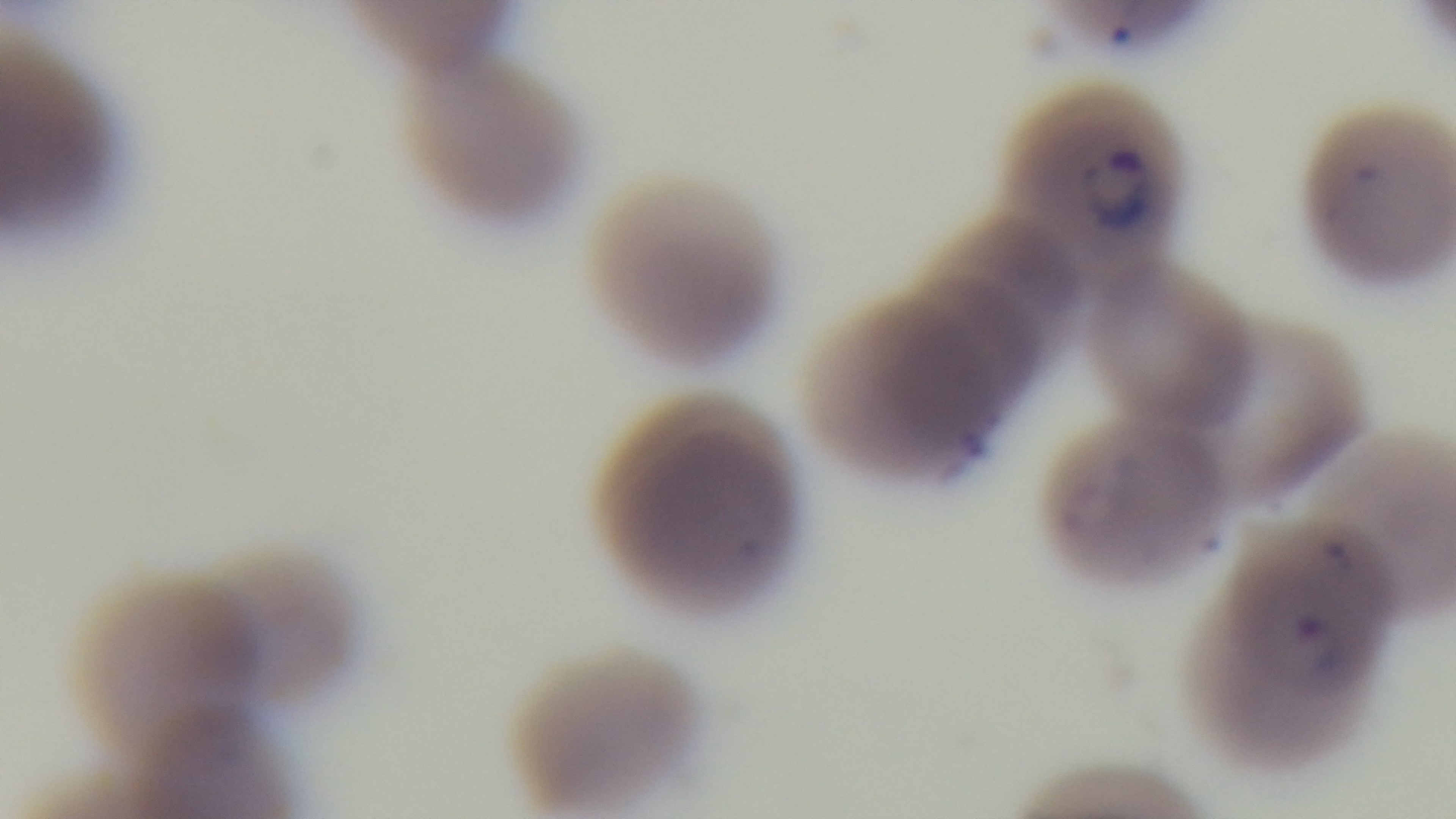
Summary:
  - Field of view: one from the slide
  - Preparation: thin smear
  - Capture: mounted 4K digital camera
  - Objective: 100x oil immersion
  - Malaria status: infected
  - Modality: light microscopy
  - Stain: Giemsa